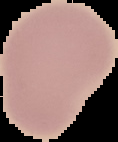

Segmented cell region on a black background. From a thin blood film. Malaria status: uninfected. Image is 118×142 pixels.